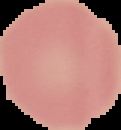
From a thin blood film. Image is 121×130 pixels. Cell region segmented out of the field of view; the surrounding area is masked to black. Malaria status: uninfected.